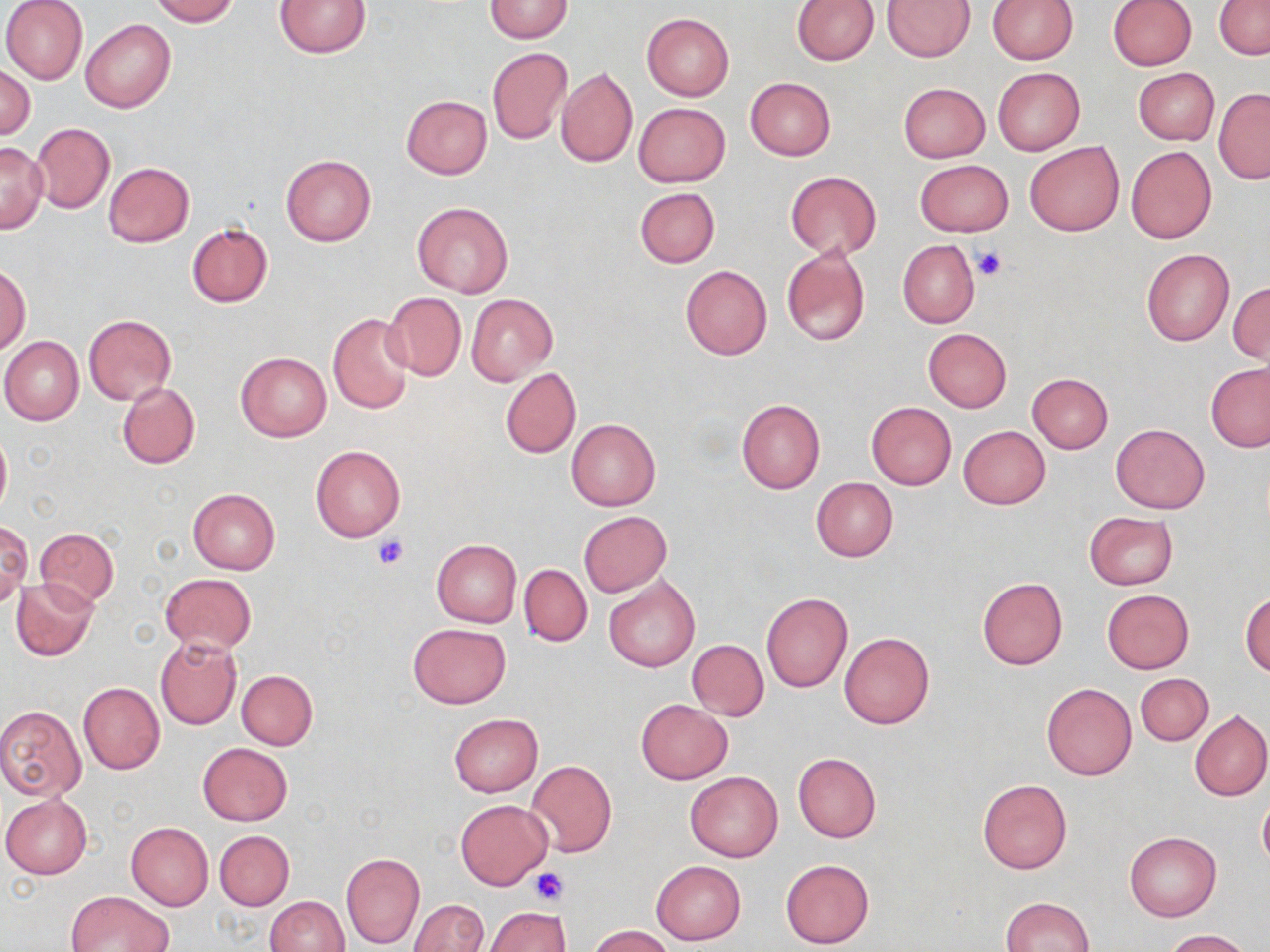 Approximate bounding boxes as (x1, y1, x2, y2) in pixels. Uninfected red blood cell locations: (1, 0, 87, 85), (148, 0, 238, 25), (276, 0, 370, 57), (792, 0, 878, 65), (883, 0, 975, 60), (988, 0, 1078, 64), (483, 1, 573, 42), (1107, 1, 1197, 69), (1215, 1, 1270, 59), (641, 13, 734, 101), (81, 19, 175, 113), (487, 48, 571, 144), (1, 66, 35, 139), (556, 67, 637, 168), (991, 68, 1085, 156), (1134, 68, 1218, 144), (745, 78, 835, 161), (898, 82, 991, 162), (1214, 89, 1270, 183), (401, 95, 492, 179), (633, 103, 730, 186), (30, 122, 115, 214), (0, 141, 46, 232), (1024, 142, 1125, 235), (1126, 145, 1218, 244), (282, 154, 375, 246), (915, 159, 1013, 236), (103, 161, 193, 247), (784, 171, 881, 259), (635, 187, 719, 267), (412, 202, 513, 298), (186, 223, 273, 308), (898, 240, 980, 327), (781, 245, 870, 347), (1141, 248, 1233, 346), (1, 264, 31, 354), (680, 265, 773, 360), (1229, 280, 1269, 366), (383, 291, 466, 381), (466, 293, 557, 385), (327, 311, 416, 415), (84, 315, 176, 405), (101, 316, 188, 471), (923, 328, 1012, 413), (2, 336, 84, 426), (235, 352, 331, 441), (1205, 362, 1270, 452), (500, 368, 581, 459), (1027, 373, 1112, 454), (117, 381, 200, 469), (736, 398, 824, 495), (865, 402, 955, 491), (566, 418, 660, 510), (1110, 424, 1210, 514), (958, 425, 1050, 509), (0, 427, 11, 519), (310, 445, 405, 542), (811, 477, 897, 562), (188, 489, 280, 575), (579, 511, 670, 596), (1084, 512, 1178, 590), (1, 519, 31, 608), (34, 528, 120, 609), (432, 539, 521, 627), (519, 564, 592, 646), (160, 573, 256, 652), (604, 574, 700, 672), (977, 576, 1067, 670), (10, 577, 98, 661), (1102, 589, 1194, 673), (761, 592, 852, 692), (1241, 593, 1270, 677), (408, 623, 510, 708), (839, 632, 934, 729), (154, 636, 242, 730), (687, 640, 769, 719), (236, 669, 317, 750), (1136, 674, 1213, 746), (78, 682, 165, 775), (1041, 683, 1138, 781), (636, 699, 733, 784), (0, 705, 87, 800), (1190, 709, 1270, 802), (449, 714, 542, 797), (198, 742, 292, 825), (793, 752, 882, 842), (526, 760, 617, 857), (685, 772, 782, 862), (977, 779, 1073, 874), (1257, 794, 1270, 870), (1, 795, 91, 879), (456, 800, 551, 889), (126, 823, 214, 911), (214, 830, 294, 909), (1124, 831, 1221, 921), (341, 852, 425, 949), (780, 859, 874, 948), (651, 860, 745, 944), (66, 891, 175, 952), (264, 896, 349, 952), (1000, 897, 1094, 952), (410, 900, 488, 952), (485, 906, 570, 952), (589, 924, 675, 951), (1166, 929, 1250, 951). Platelet locations: (973, 247, 1006, 281), (374, 535, 408, 568), (532, 867, 568, 906). Slide-level diagnosis: no evidence of blood parasites. May-Grünwald-Giemsa stain. Optical microscopy. Image is 1270×952 pixels. Thin blood smear. One field of a larger specimen. 1000x magnification.